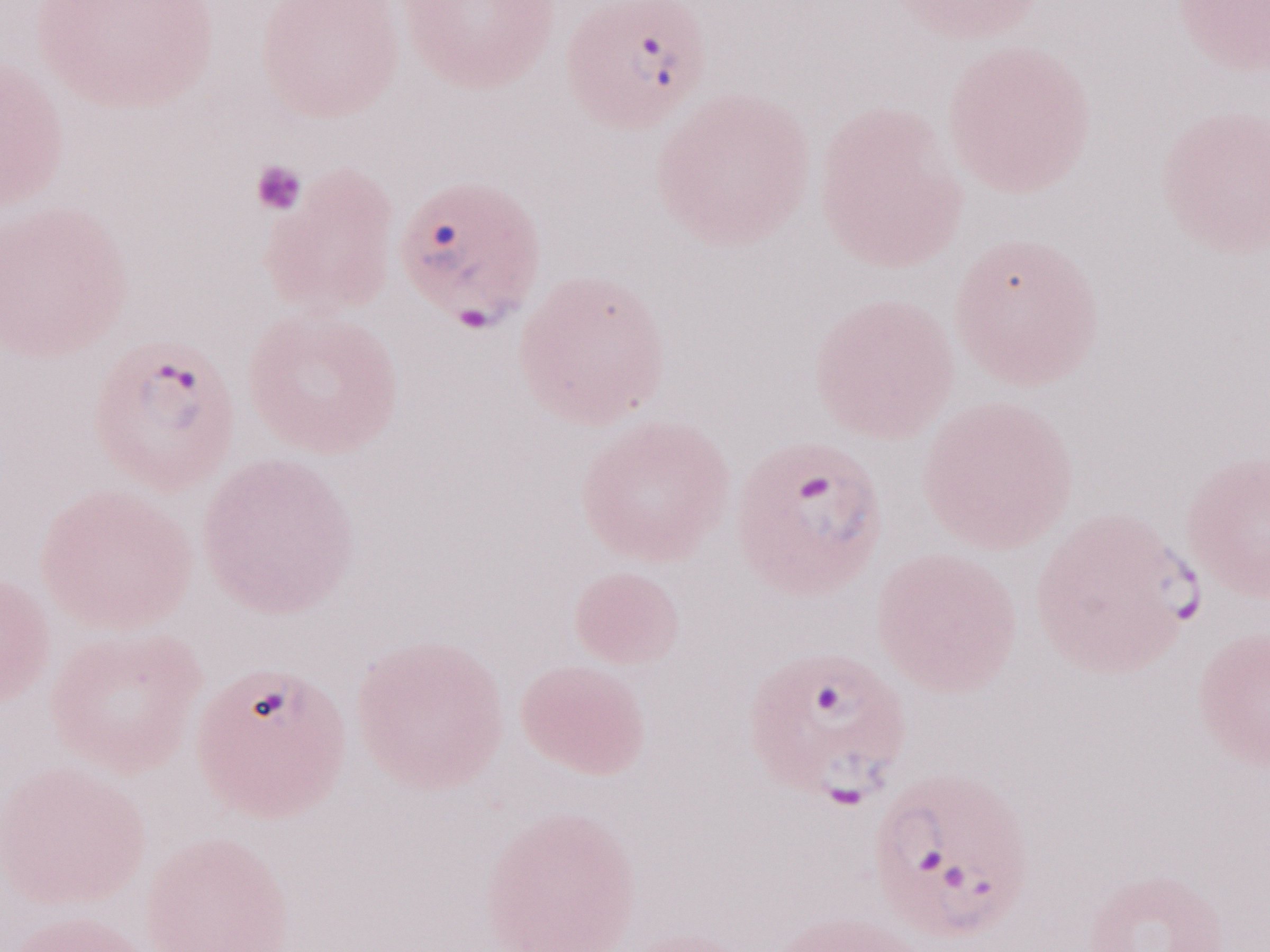
Olympus BX43 microscope and DP73 digital camera. May-Grünwald-Giemsa stain. One field of this slide. Thin blood smear. Malaria diagnosis (patient-level): positive. Image is 1270×952 pixels. 1,000x magnification.